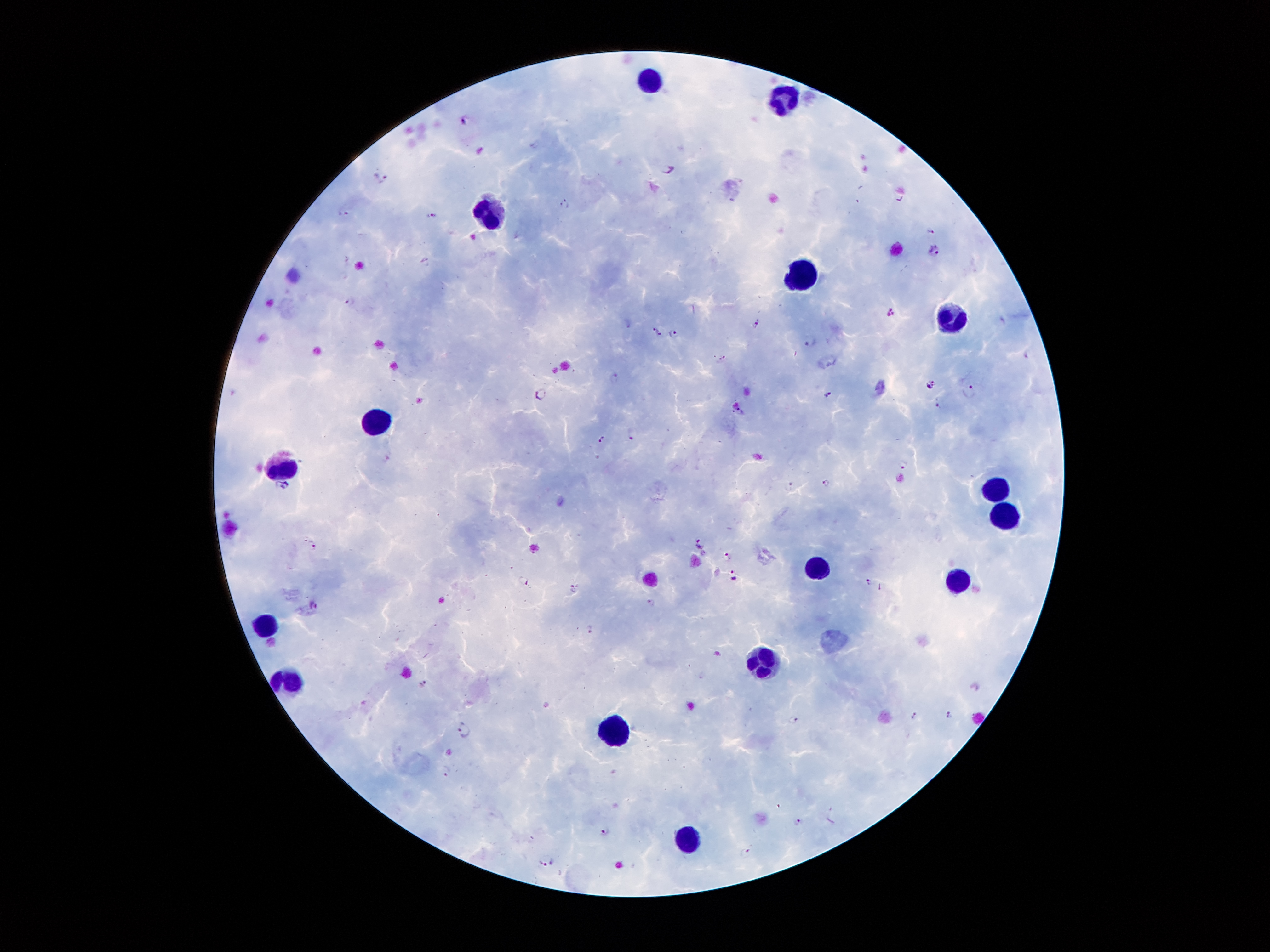
coordinate format = approximate centers as [x, y] in pixels
Plasmodium parasite locations = [463, 118], [669, 171], [382, 177], [565, 203], [347, 212], [435, 215], [930, 228], [934, 250], [350, 302], [891, 311], [758, 323], [656, 331], [674, 334], [810, 341], [1028, 353], [724, 357], [614, 378], [930, 384], [971, 391], [539, 394], [828, 394], [939, 406], [741, 410], [633, 435], [602, 439], [903, 465], [825, 483], [791, 484], [282, 485], [313, 543], [701, 543], [727, 556], [731, 573], [525, 581], [869, 581], [574, 588], [651, 602], [314, 606], [590, 628], [718, 653], [424, 683], [949, 714], [914, 715], [793, 720], [463, 729], [797, 820], [605, 831], [746, 853], [545, 860]
leukocyte locations = [653, 83], [787, 94], [492, 211], [803, 273], [955, 318], [379, 416], [286, 466], [1003, 488], [1001, 515], [820, 567], [963, 579], [265, 624], [762, 664], [296, 682], [611, 725], [690, 838]
capture = smartphone camera through the microscope eyepiece
preparation = thick blood film
image size = 1270×952 pixels
patient malaria status = infected with Plasmodium falciparum
magnification = 100x
stain = Giemsa
field of view = one from this slide